Name the parasite shown.
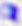

This is Toxoplasma gondii.

Captured at 400x magnification. Micrograph.